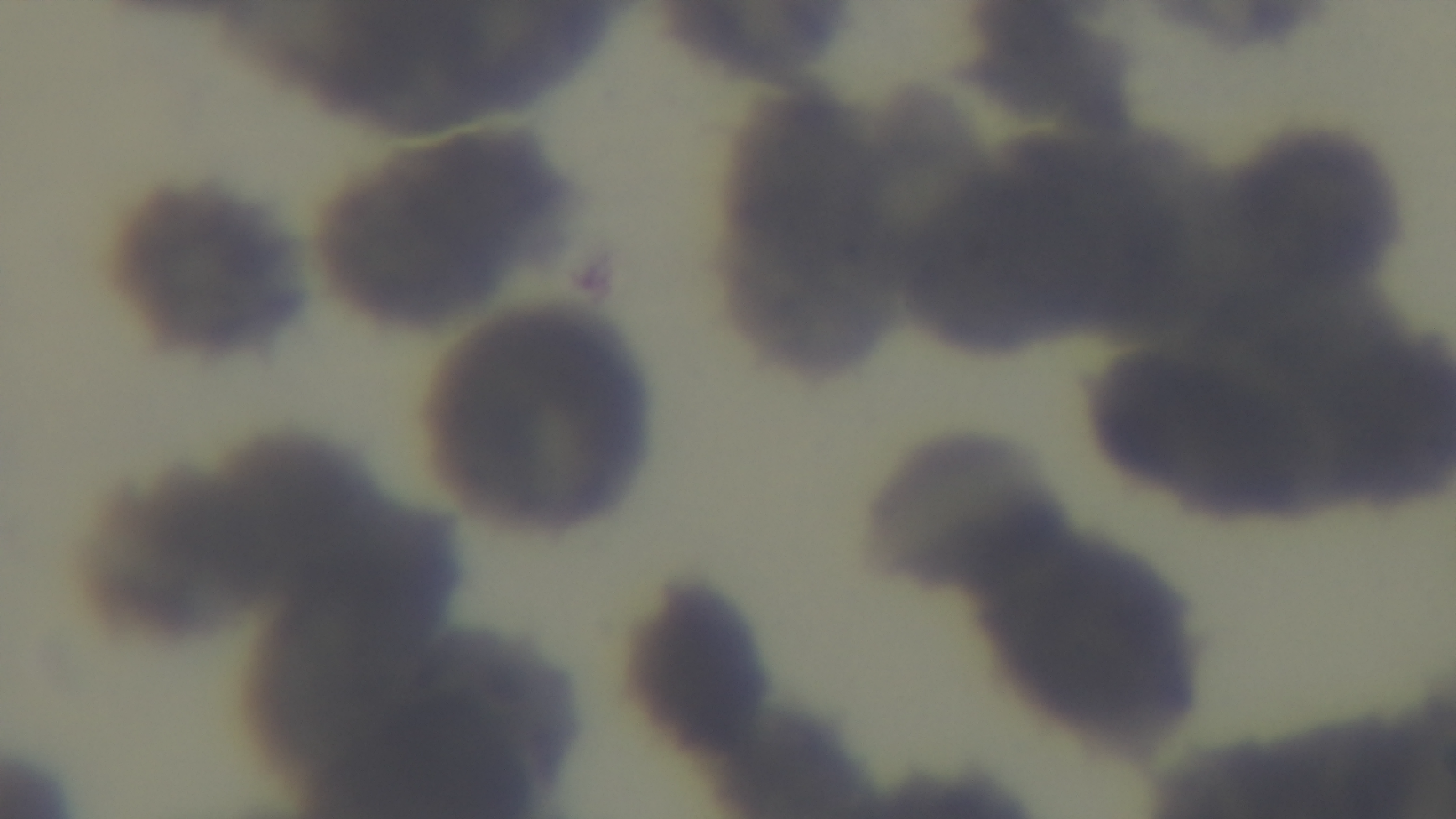
stain = Giemsa
field of view = one from the slide
preparation = thin smear
capture = mounted 4K digital camera
malaria status = uninfected
objective = 100x oil immersion
modality = light microscopy